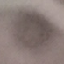

malaria_status: uninfected
stain: Giemsa
preparation: thin smear
capture: smartphone camera at the microscope eyepiece
image_type: automatically extracted cell patch, resized to 64 × 64 pixels